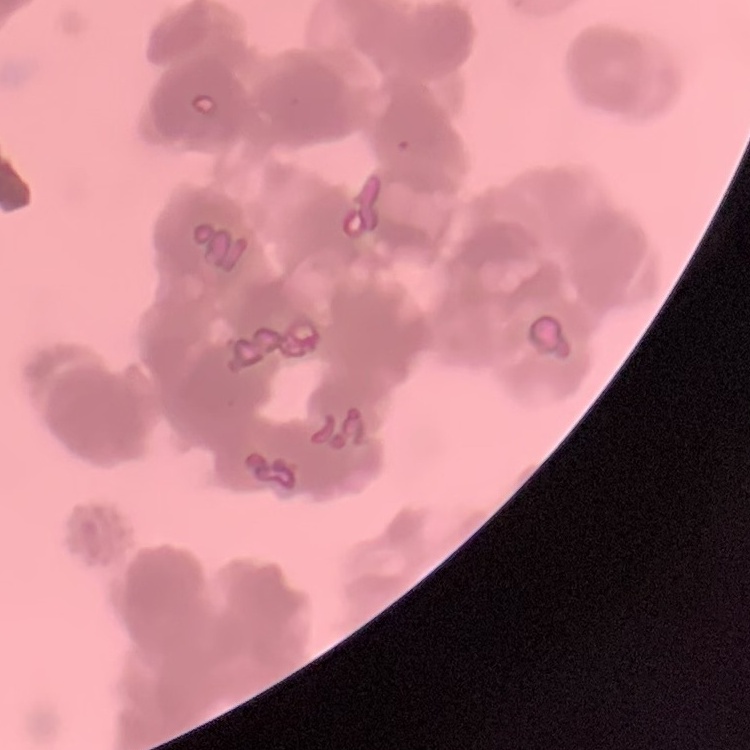

erythrocyte_morphology: rouleaux formation
image_type: one tile cut from a larger photomicrograph
preparation: thin peripheral smear
stain: Field's or Giemsa